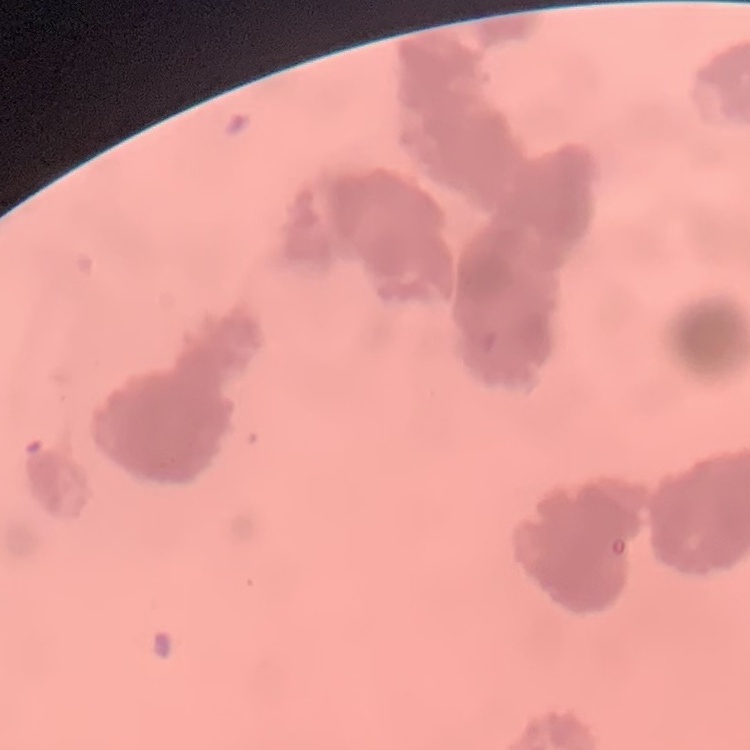
The erythrocytes exhibit rouleaux formation. One tile cut from a larger photomicrograph. Thin peripheral smear. Field's or Giemsa stain.